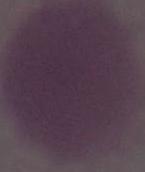
Summary:
  - Modality: photomicrograph
  - Identification: red blood cell
  - Magnification: 1000x